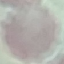
Summary:
  - Malaria status: uninfected
  - Image type: automatically extracted cell patch, resized to 64 × 64 pixels
  - Stain: Giemsa
  - Preparation: thin blood smear
  - Capture: smartphone camera at the microscope eyepiece